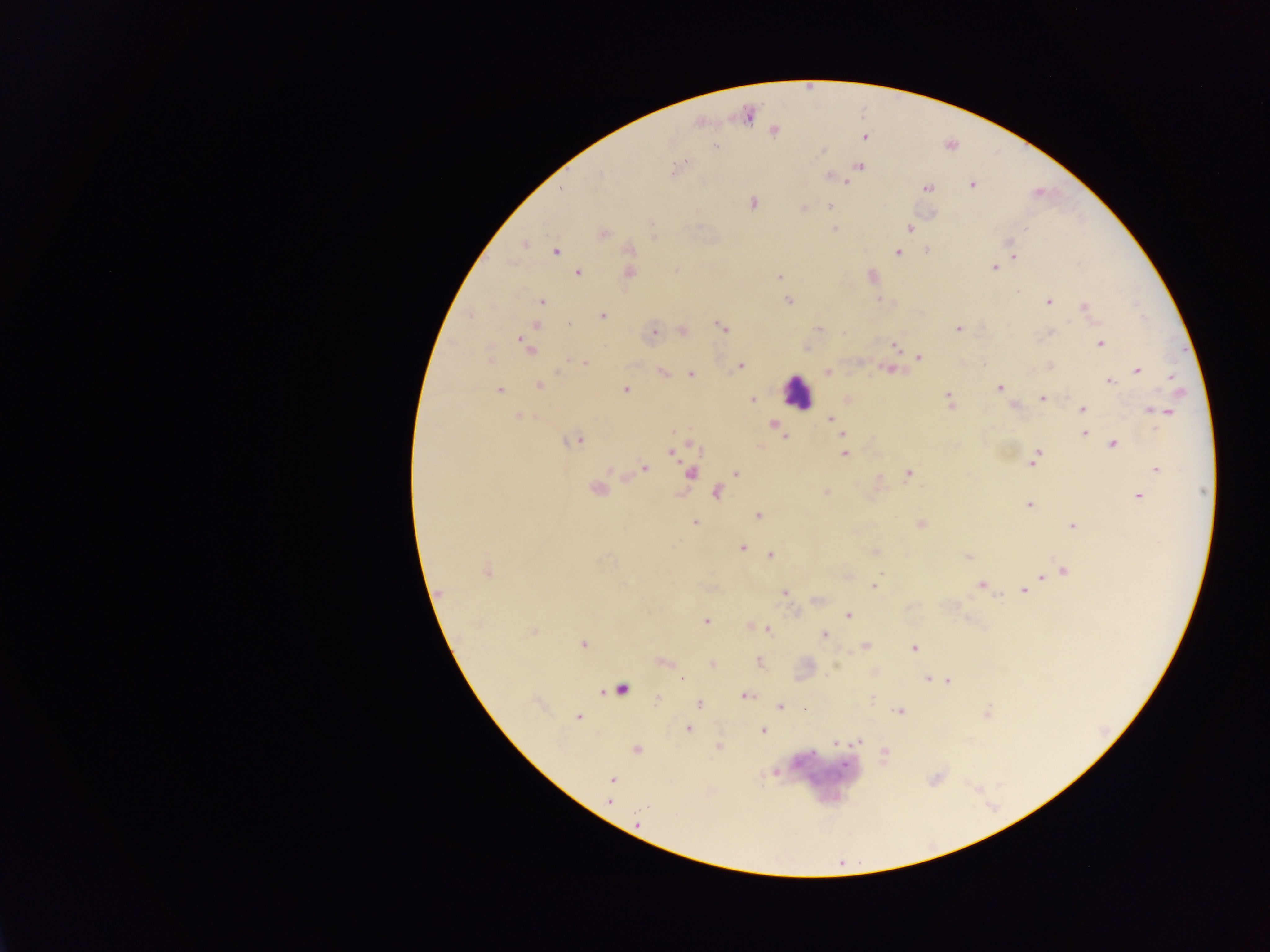

malaria parasite locations = approximate centers as x y in pixels: 748 115; 774 131; 865 136; 715 146; 822 150; 686 160; 682 165; 859 167; 674 171; 600 174; 829 177; 844 181; 971 184; 927 188; 562 189; 752 202; 830 206; 804 208; 910 228; 835 229; 604 233; 1009 242; 525 245; 630 249; 927 250; 556 251; 898 252; 1013 255; 993 268; 676 270; 630 272; 578 273; 872 276; 779 278; 879 299; 541 302; 789 302; 1049 302; 1084 307; 602 316; 535 326; 722 326; 819 329; 958 329; 683 331; 654 332; 845 334; 1100 343; 896 347; 529 348; 919 357; 585 362; 984 365; 741 366; 1050 367; 889 370; 1137 371; 663 373; 827 373; 690 374; 1171 377; 1110 381; 538 386; 999 388; 625 389; 500 390; 948 398; 1042 398; 753 400; 1014 406; 1083 409; 1163 411; 519 416; 831 419; 774 424; 842 434; 1084 434; 783 436; 574 441; 1113 445; 672 452; 844 453; 1035 457; 1032 463; 644 468; 1157 469; 690 473; 736 473; 907 474; 597 489; 717 492; 826 493; 1139 496; 1029 505; 759 516; 695 523; 921 524; 1072 526; 742 547; 876 552; 770 555; 969 557; 1064 571; 486 572; 880 573; 1042 577; 981 585; 874 586; 1024 590; 785 592; 442 594; 849 616; 706 621; 751 626; 767 629; 534 632; 825 636; 583 644; 865 646; 914 648; 664 662; 759 662; 712 664; 928 680; 949 682; 745 696; 657 698; 699 704; 779 706; 804 708; 900 711; 987 713; 577 717; 688 729; 763 731; 858 741; 835 743; 718 746; 637 750; 885 753; 612 779; 609 801
leukocyte locations = approximate centers as x y in pixels: 797 392; 619 688
preparation = thick blood film
country = Ghana
image size = 1270×952 pixels
capture = mobile-phone photograph through a microscope
field of view = single